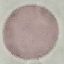
Result: no malaria parasites detected. Cell patch, automatically extracted from a larger field of view and resized to 64 × 64 pixels. Thin smear of blood. Giemsa-stained preparation. Acquired by smartphone through the microscope eyepiece.